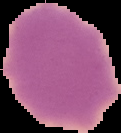
Segmented cell region on a black background. From a thin blood smear. Result: no malaria parasites seen. Image is 121×133 pixels.